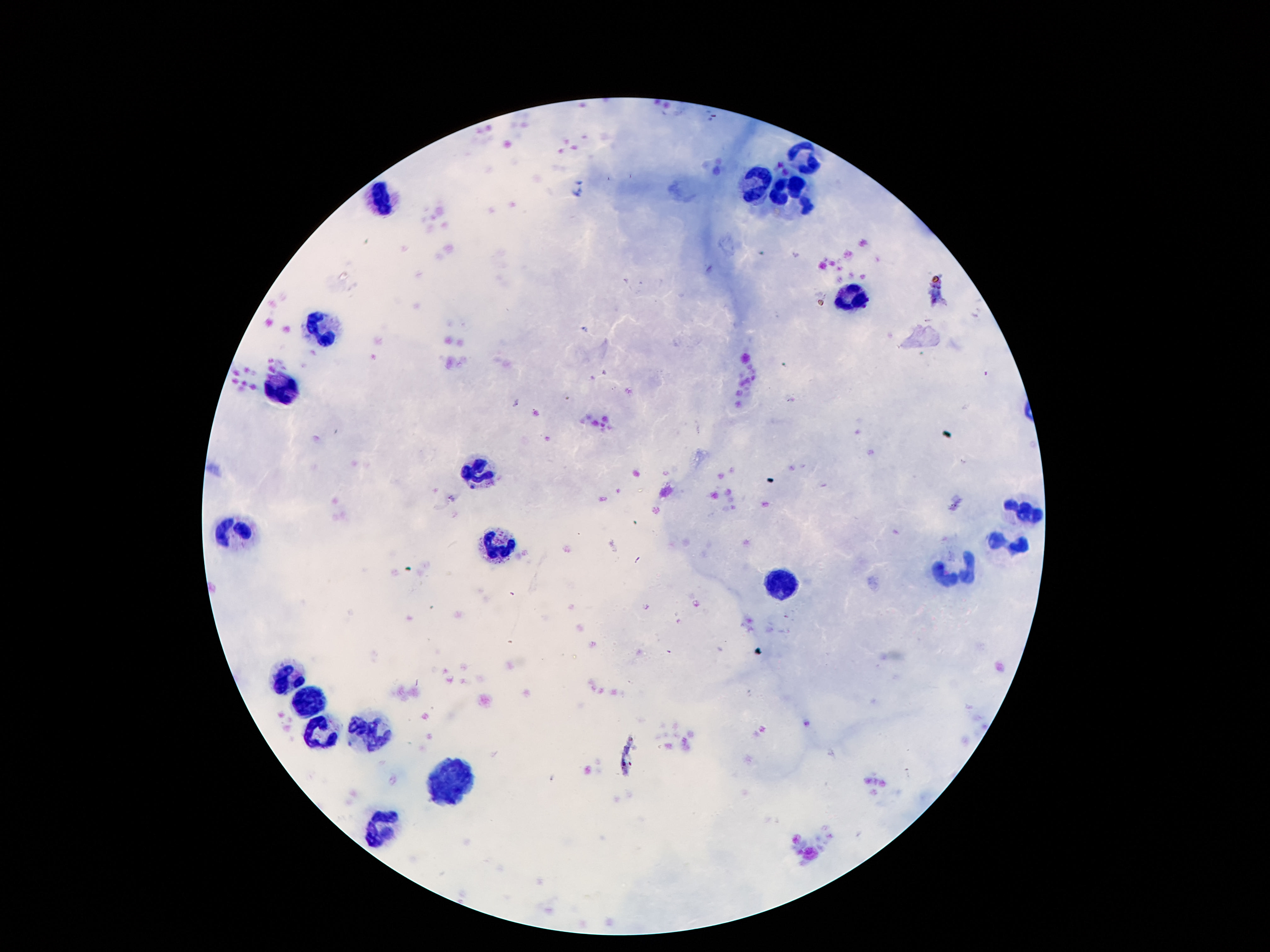
Approximate centers as {x, y} in pixels. Leukocyte locations: {804, 155}, {752, 184}, {381, 196}, {787, 197}, {849, 293}, {327, 333}, {278, 381}, {475, 473}, {1022, 512}, {241, 532}, {1009, 540}, {495, 543}, {955, 572}, {784, 584}, {288, 675}, {310, 698}, {367, 725}, {322, 732}, {446, 781}, {381, 827}. Patient malaria status: not infected. Photographed through the microscope eyepiece with a smartphone camera. 100x magnification. Giemsa stain. Thick blood smear. One field from this slide. Image is 1270×952 pixels.